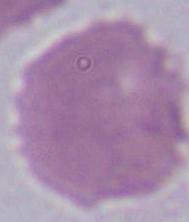
An erythrocyte is seen. Captured at 1000x magnification. Photomicrograph.